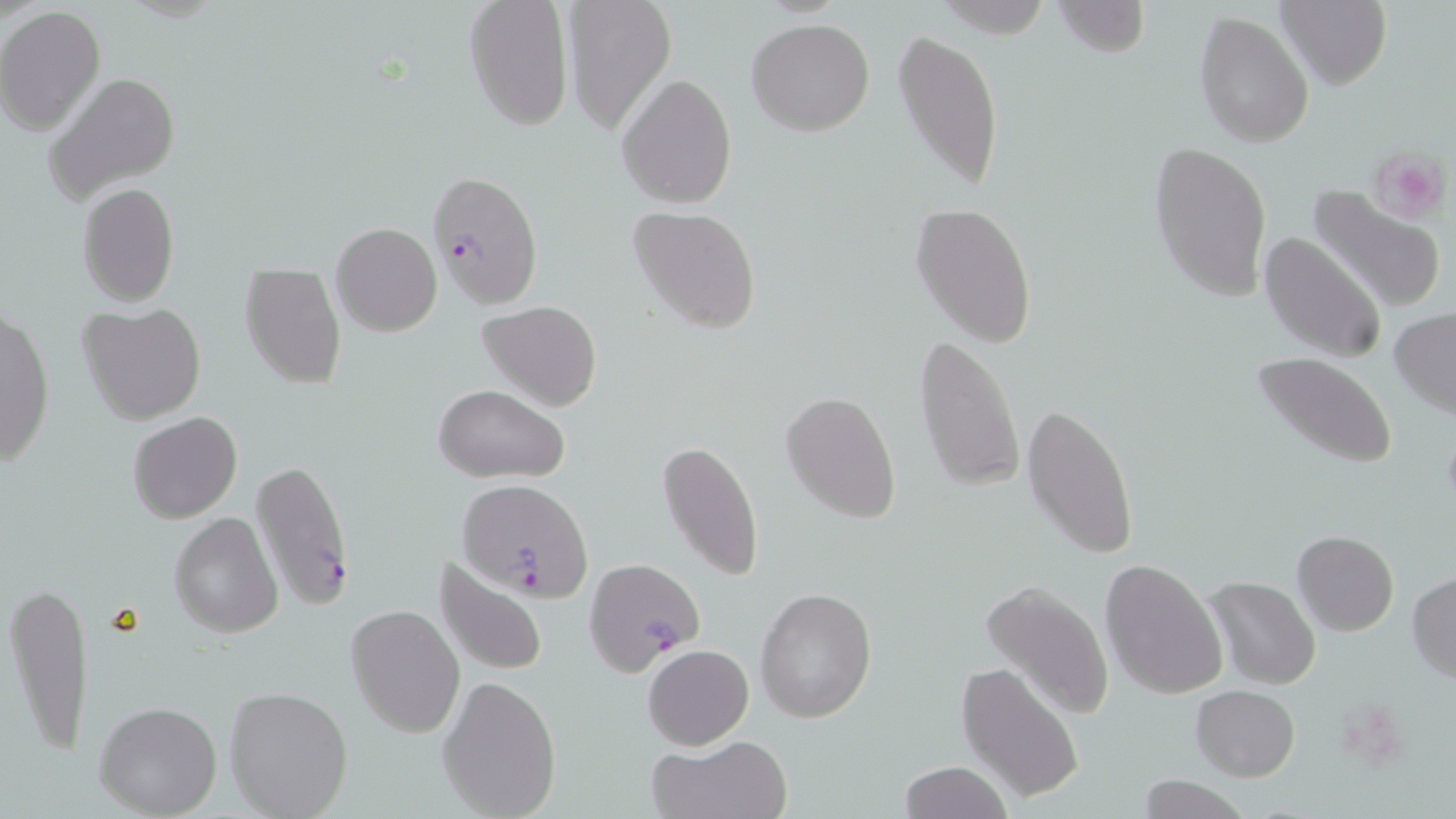

Summary:
  - Coordinate format: approximate bounding boxes as named x1/y1/x2/y2 corners in pixels
  - Plasmodium falciparum-infected red blood cell locations: (x1=427, y1=170, x2=544, y2=308), (x1=252, y1=458, x2=356, y2=612), (x1=459, y1=480, x2=594, y2=600), (x1=585, y1=558, x2=704, y2=674)
  - Uninfected red blood cell locations: (x1=561, y1=0, x2=678, y2=135), (x1=1053, y1=0, x2=1152, y2=59), (x1=1277, y1=0, x2=1391, y2=90), (x1=463, y1=1, x2=574, y2=131), (x1=0, y1=6, x2=107, y2=137), (x1=1194, y1=10, x2=1313, y2=149), (x1=746, y1=17, x2=875, y2=136), (x1=893, y1=28, x2=1004, y2=198), (x1=44, y1=70, x2=181, y2=205), (x1=617, y1=72, x2=738, y2=211), (x1=1149, y1=138, x2=1271, y2=304), (x1=76, y1=182, x2=180, y2=308), (x1=1306, y1=186, x2=1446, y2=316), (x1=910, y1=202, x2=1039, y2=345), (x1=627, y1=205, x2=763, y2=335), (x1=331, y1=221, x2=441, y2=337), (x1=1258, y1=229, x2=1386, y2=365), (x1=240, y1=262, x2=347, y2=391), (x1=477, y1=302, x2=603, y2=412), (x1=78, y1=303, x2=207, y2=427), (x1=1390, y1=307, x2=1456, y2=417), (x1=1, y1=309, x2=55, y2=466), (x1=913, y1=334, x2=1025, y2=492), (x1=1252, y1=351, x2=1399, y2=469), (x1=431, y1=383, x2=570, y2=483), (x1=781, y1=389, x2=902, y2=523), (x1=1023, y1=401, x2=1138, y2=561), (x1=128, y1=412, x2=242, y2=524), (x1=656, y1=440, x2=767, y2=586), (x1=169, y1=512, x2=282, y2=639), (x1=1292, y1=531, x2=1398, y2=635), (x1=433, y1=556, x2=552, y2=678), (x1=1101, y1=559, x2=1228, y2=701), (x1=376, y1=566, x2=518, y2=711), (x1=1408, y1=573, x2=1456, y2=683), (x1=1206, y1=576, x2=1321, y2=690), (x1=979, y1=578, x2=1113, y2=721), (x1=5, y1=579, x2=94, y2=759), (x1=755, y1=586, x2=877, y2=724), (x1=346, y1=604, x2=465, y2=739), (x1=642, y1=644, x2=754, y2=749), (x1=956, y1=660, x2=1086, y2=804), (x1=437, y1=675, x2=563, y2=816), (x1=223, y1=686, x2=354, y2=819), (x1=1192, y1=686, x2=1300, y2=780), (x1=94, y1=700, x2=223, y2=817), (x1=649, y1=736, x2=792, y2=819), (x1=898, y1=761, x2=1014, y2=819), (x1=1133, y1=776, x2=1251, y2=818)
  - Platelet locations: (x1=1370, y1=149, x2=1449, y2=223)
  - Slide-level diagnosis: Plasmodium falciparum
  - Preparation: thin blood film
  - Field of view: one of a larger specimen
  - Image size: 1456×819 pixels
  - Modality: optical microscopy
  - Magnification: 1000x
  - Stain: May-Grünwald-Giemsa